Assess this cell for malaria.
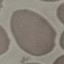

It is uninfected.

capture: smartphone camera at the microscope eyepiece
stain: Giemsa
image_type: automatically extracted cell patch, resized to 64 × 64 pixels
preparation: thin blood film